Give the preparation type.
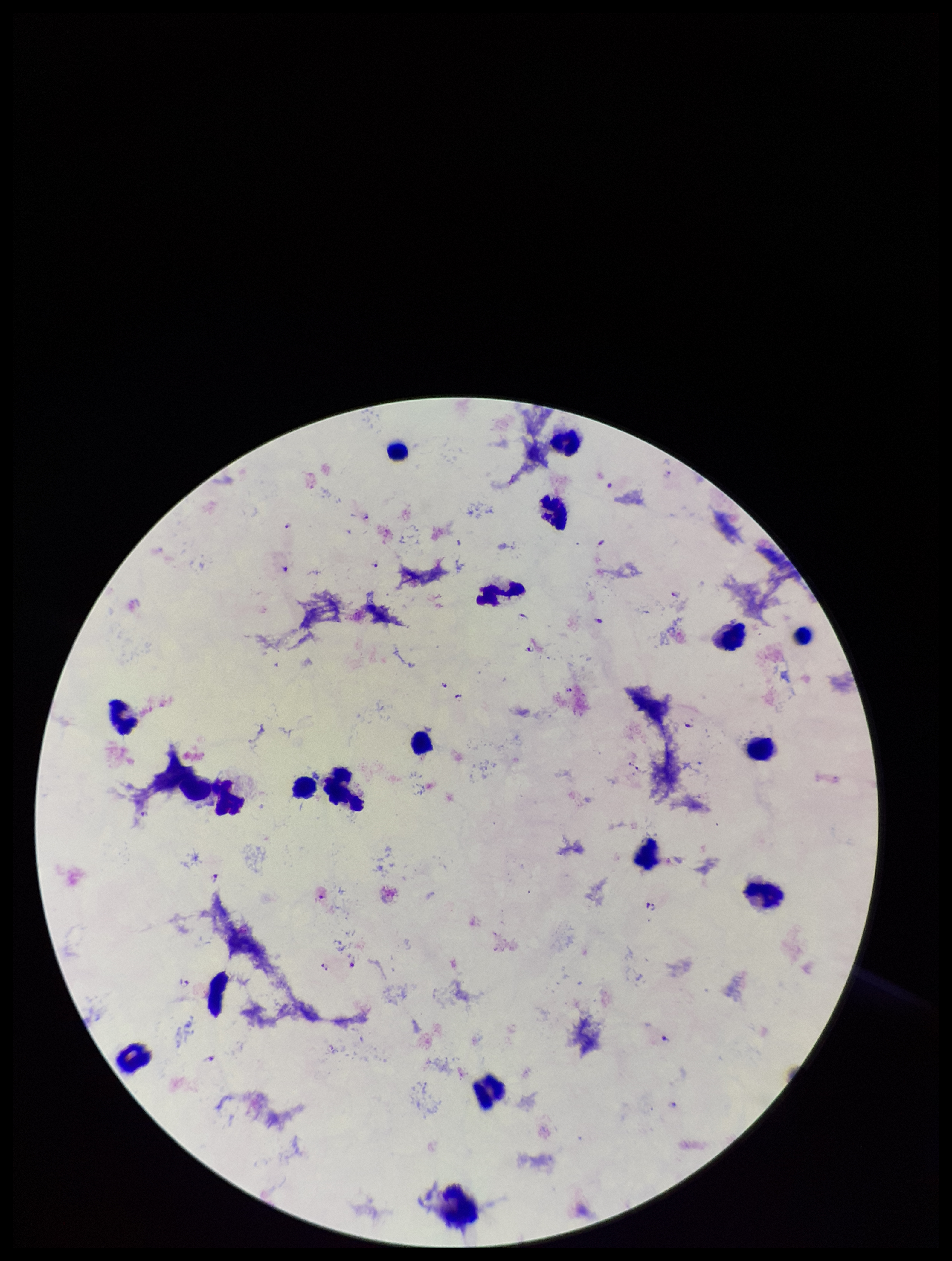
A thick smear.

stain = Giemsa
image size = 952×1261 pixels
species reported for this patient = Plasmodium falciparum
field of view = single
capture = smartphone photograph through the microscope eyepiece
Plasmodium parasites = identified
leukocyte count = 18
patient malaria status = positive
parasite count = 27